Name the cell type shown.
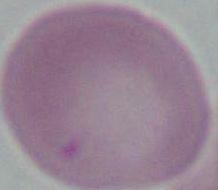

An erythrocyte.

Summary:
  - Magnification: 1000x
  - Modality: photomicrograph